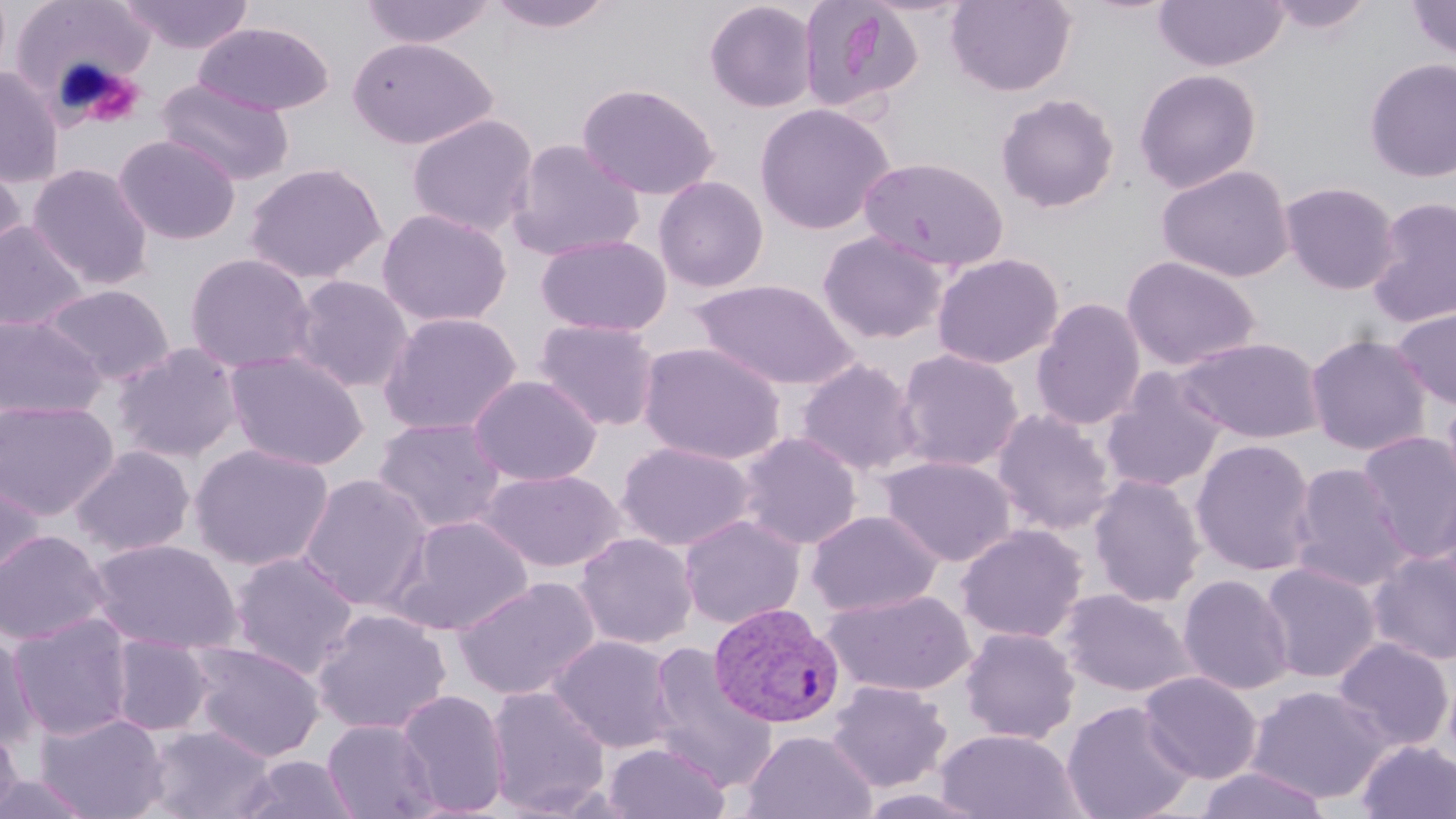

Summary:
  - Coordinate format: approximate bounding boxes as (x1,y1)-(x2,y2) corner pairs in pixels
  - Plasmodium vivax-infected red blood cell locations: (709,602)-(845,728)
  - Uninfected red blood cell locations: (118,0)-(255,55), (359,0)-(496,48), (485,0)-(618,33), (797,0)-(922,113), (946,0)-(1076,96), (1153,0)-(1287,72), (1264,0)-(1378,35), (1405,0)-(1456,61), (10,1)-(155,110), (704,1)-(818,113), (194,22)-(334,116), (346,37)-(497,149), (1363,57)-(1456,182), (0,66)-(65,188), (1134,68)-(1262,193), (155,78)-(294,186), (576,82)-(721,200), (995,92)-(1121,214), (754,101)-(896,235), (406,113)-(538,237), (114,134)-(241,245), (507,139)-(644,262), (0,156)-(27,276), (858,156)-(1010,273), (243,161)-(387,284), (27,163)-(153,290), (1156,164)-(1295,283), (652,175)-(769,293), (1279,181)-(1401,294), (1366,196)-(1456,327), (376,208)-(512,327), (0,220)-(89,332), (817,230)-(949,345), (535,233)-(672,337), (184,253)-(317,374), (931,253)-(1065,370), (1121,255)-(1261,372), (290,275)-(413,392), (690,277)-(860,390), (40,283)-(174,386), (1031,297)-(1146,431), (1391,306)-(1456,411), (379,312)-(521,436), (0,314)-(106,420), (534,318)-(661,431), (1304,334)-(1433,456), (1173,336)-(1326,444), (638,342)-(787,466), (113,343)-(244,463), (894,348)-(1025,472), (225,350)-(369,471), (795,358)-(923,476), (1101,369)-(1228,493), (468,374)-(602,486), (1440,389)-(1456,511), (0,399)-(118,520), (992,408)-(1116,534), (372,417)-(507,535), (1356,430)-(1456,563), (736,431)-(862,550), (1191,438)-(1317,576), (617,441)-(756,551), (189,443)-(334,571), (70,445)-(195,558), (879,456)-(1017,566), (1288,462)-(1413,592), (479,468)-(624,572), (297,472)-(433,612), (1088,474)-(1206,608), (0,475)-(45,590), (1431,479)-(1456,608), (806,509)-(943,617), (388,514)-(534,636), (678,514)-(806,629), (955,524)-(1088,644), (0,529)-(111,646), (574,532)-(698,649), (89,539)-(242,655), (228,550)-(360,679), (1367,551)-(1456,666), (1260,562)-(1380,683), (1178,574)-(1294,695), (454,575)-(601,701), (823,588)-(976,697), (1059,588)-(1194,698), (311,607)-(452,736), (9,613)-(135,741), (959,626)-(1080,744), (0,630)-(39,753), (549,634)-(680,753), (109,635)-(212,736), (1331,637)-(1454,752), (186,642)-(325,761), (646,642)-(775,790), (1138,671)-(1262,784), (826,680)-(952,793), (1245,684)-(1391,804), (486,685)-(611,816), (396,688)-(510,816), (1061,700)-(1197,819), (37,712)-(169,819), (322,719)-(441,819), (0,724)-(24,818), (145,724)-(276,819), (935,728)-(1085,819), (742,729)-(876,819), (1356,740)-(1456,819), (602,742)-(730,819), (233,754)-(360,818), (1194,766)-(1332,819), (0,771)-(98,817)
  - Slide-level diagnosis: Plasmodium vivax
  - Stain: May-Grünwald-Giemsa
  - Preparation: thin blood smear
  - Field of view: single
  - Modality: optical microscopy
  - Magnification: 1000x
  - Image size: 1456×819 pixels